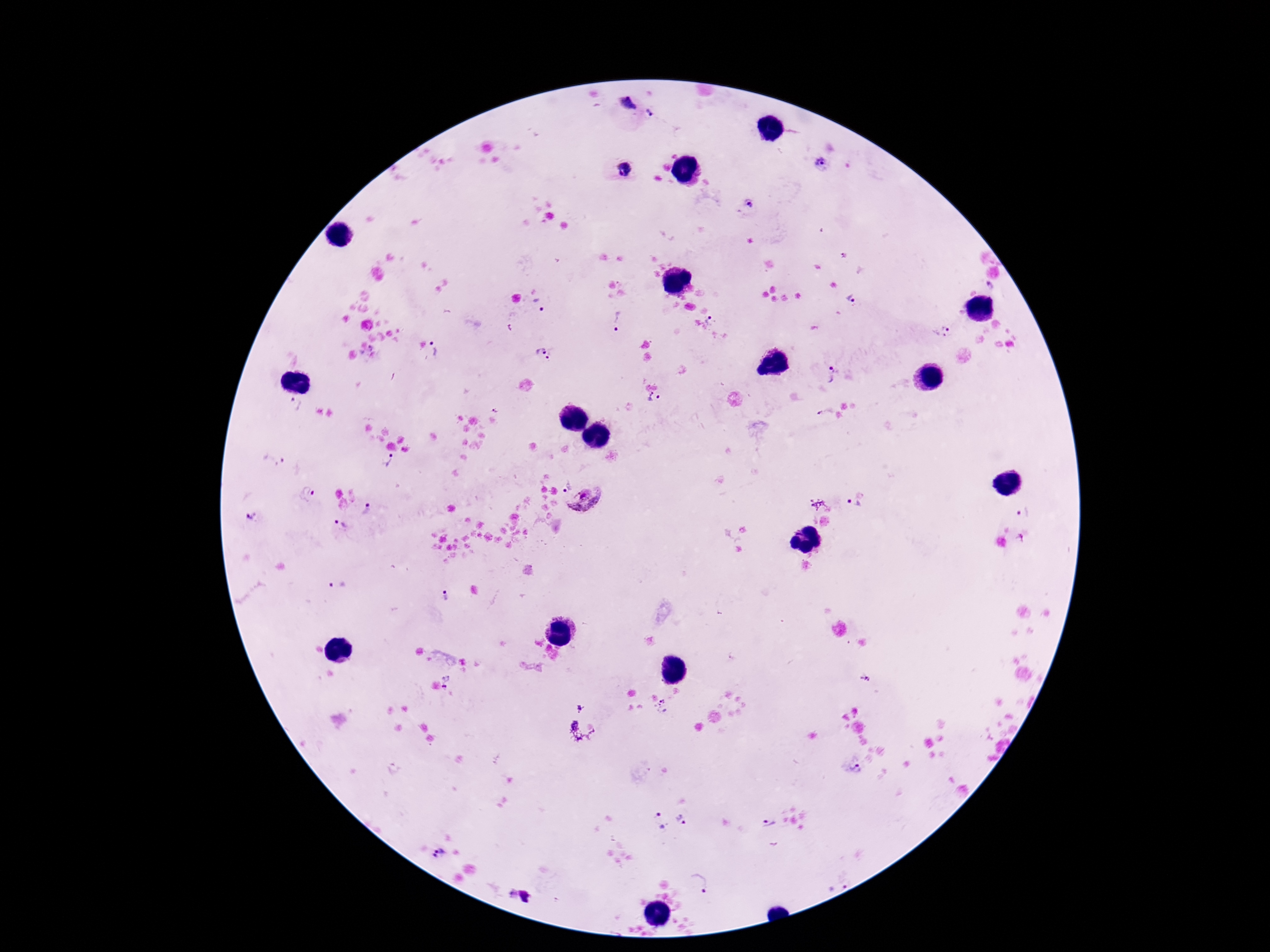

{
  "patient_malaria_status": "positive",
  "plasmodium_parasite_locations": "approximate centers as [x, y] in pixels: [629, 103], [652, 115], [822, 164], [626, 170], [751, 204], [845, 255], [990, 285], [851, 299], [539, 303], [617, 320], [712, 320], [941, 331], [438, 349], [541, 351], [553, 354], [829, 374], [654, 400], [295, 404], [497, 407], [825, 412], [275, 458], [389, 461], [566, 485], [307, 495], [586, 503], [854, 504], [365, 510], [1021, 513], [253, 517], [340, 525], [337, 585], [445, 596], [450, 683], [661, 706], [581, 709], [855, 768], [682, 819], [658, 821], [768, 825], [438, 855], [698, 882], [513, 893], [526, 897]",
  "image_size": "1270×952 pixels",
  "preparation": "thick blood film",
  "stain": "Giemsa",
  "field_of_view": "single",
  "magnification": "100x",
  "capture": "smartphone camera through the microscope eyepiece"
}